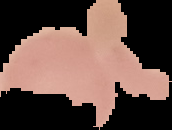

Segmented cell region on a black background. Image is 172×130 pixels. From a thin blood film. Result: negative for malaria parasites.